Outline each Plasmodium falciparum-infected red blood cell.
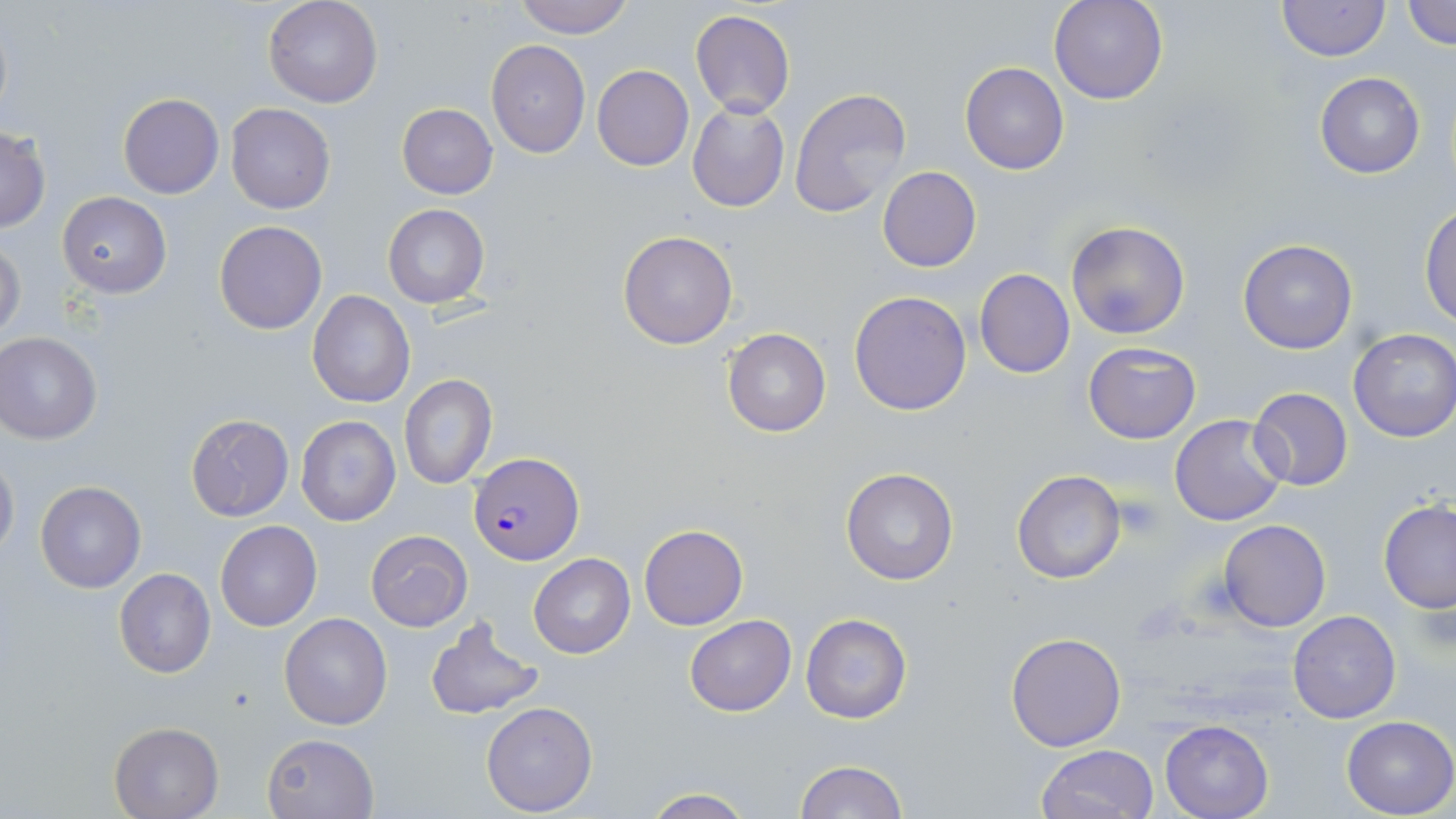
Approximate bounding boxes as named x1/y1/x2/y2 corners in pixels.
Plasmodium falciparum-infected red blood cells: (x1=468, y1=454, x2=583, y2=564).

Summary:
  - Platelet locations: (x1=1112, y1=494, x2=1164, y2=540)
  - Uninfected red blood cell locations: (x1=263, y1=0, x2=383, y2=108), (x1=513, y1=0, x2=635, y2=38), (x1=1048, y1=0, x2=1168, y2=105), (x1=1402, y1=0, x2=1456, y2=49), (x1=1276, y1=1, x2=1389, y2=62), (x1=690, y1=9, x2=796, y2=119), (x1=486, y1=39, x2=591, y2=158), (x1=959, y1=62, x2=1070, y2=175), (x1=592, y1=64, x2=693, y2=170), (x1=1315, y1=71, x2=1424, y2=179), (x1=789, y1=87, x2=913, y2=219), (x1=117, y1=93, x2=223, y2=198), (x1=686, y1=101, x2=790, y2=214), (x1=397, y1=103, x2=498, y2=199), (x1=226, y1=104, x2=335, y2=214), (x1=0, y1=127, x2=51, y2=233), (x1=876, y1=166, x2=983, y2=273), (x1=57, y1=192, x2=171, y2=298), (x1=383, y1=204, x2=490, y2=309), (x1=1420, y1=206, x2=1456, y2=328), (x1=213, y1=220, x2=327, y2=335), (x1=1065, y1=220, x2=1190, y2=340), (x1=617, y1=230, x2=738, y2=349), (x1=1237, y1=239, x2=1358, y2=354), (x1=0, y1=240, x2=25, y2=344), (x1=975, y1=269, x2=1075, y2=378), (x1=307, y1=290, x2=414, y2=408), (x1=848, y1=290, x2=972, y2=416), (x1=721, y1=326, x2=831, y2=438), (x1=1349, y1=328, x2=1456, y2=443), (x1=0, y1=330, x2=103, y2=443), (x1=1083, y1=341, x2=1201, y2=444), (x1=399, y1=376, x2=497, y2=489), (x1=1247, y1=386, x2=1353, y2=492), (x1=186, y1=414, x2=293, y2=521), (x1=1170, y1=414, x2=1290, y2=527), (x1=295, y1=415, x2=402, y2=527), (x1=0, y1=451, x2=19, y2=560), (x1=840, y1=467, x2=960, y2=587), (x1=1012, y1=470, x2=1125, y2=584), (x1=36, y1=481, x2=146, y2=593), (x1=1378, y1=500, x2=1456, y2=613), (x1=1218, y1=519, x2=1330, y2=632), (x1=215, y1=521, x2=322, y2=631), (x1=639, y1=524, x2=747, y2=629), (x1=365, y1=530, x2=473, y2=631), (x1=529, y1=553, x2=635, y2=658), (x1=115, y1=569, x2=216, y2=678), (x1=1287, y1=610, x2=1401, y2=724), (x1=278, y1=612, x2=393, y2=730), (x1=801, y1=614, x2=912, y2=723), (x1=685, y1=615, x2=796, y2=716), (x1=424, y1=618, x2=545, y2=720), (x1=1005, y1=632, x2=1126, y2=752), (x1=481, y1=702, x2=598, y2=816), (x1=1341, y1=716, x2=1455, y2=818), (x1=1159, y1=720, x2=1273, y2=818), (x1=110, y1=722, x2=223, y2=818), (x1=262, y1=731, x2=380, y2=819), (x1=1035, y1=744, x2=1161, y2=819), (x1=794, y1=760, x2=908, y2=819), (x1=639, y1=790, x2=755, y2=818)
  - Slide-level diagnosis: Plasmodium falciparum
  - Modality: optical microscopy
  - Image size: 1456×819 pixels
  - Stain: May-Grünwald-Giemsa
  - Field of view: single
  - Magnification: 1000x
  - Preparation: thin blood smear